Locate every blood parasite and identify its species.
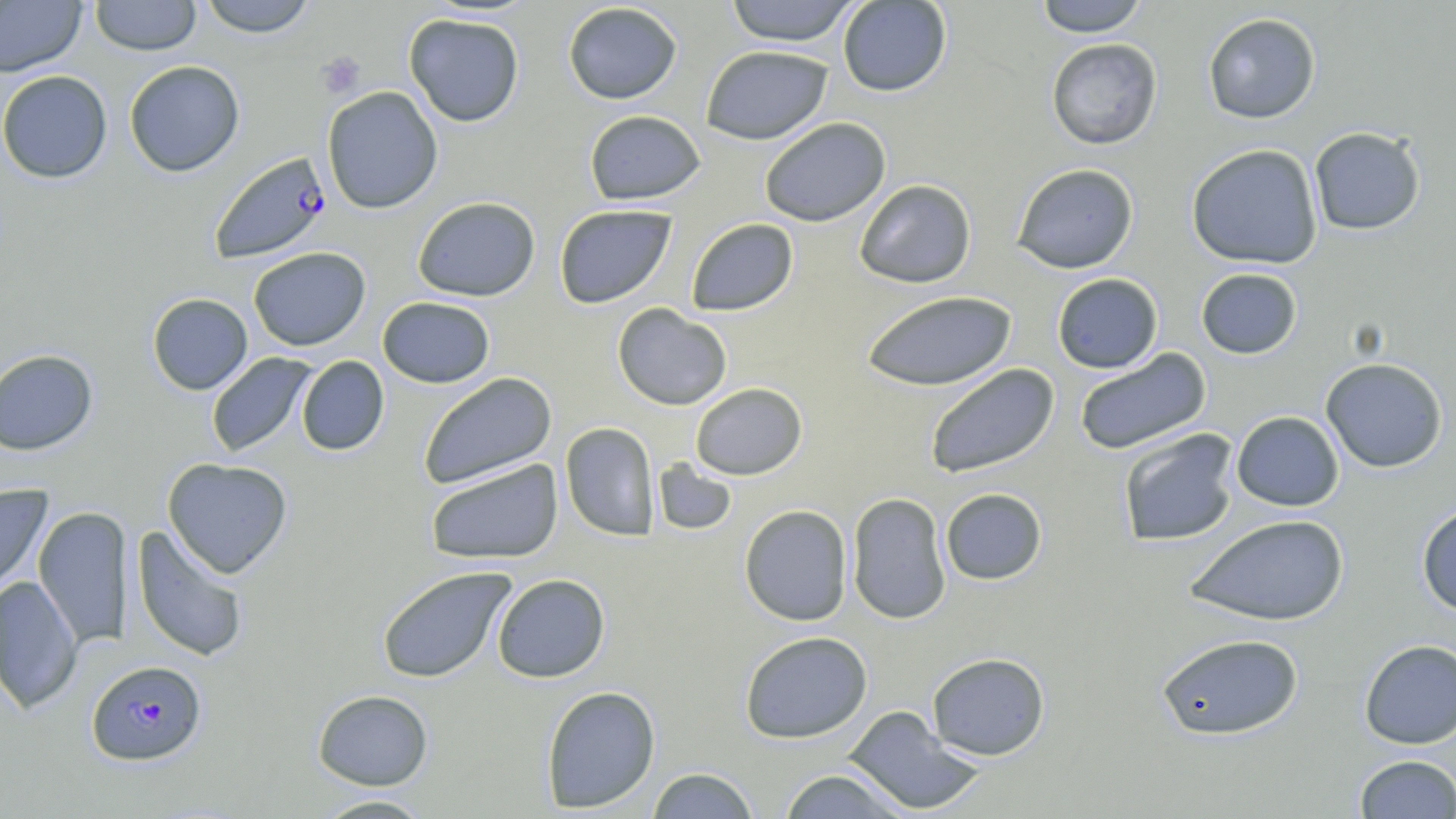
Approximate bounding boxes as named x1/y1/x2/y2 corners in pixels.
Plasmodium falciparum-infected red blood cells: (x1=208, y1=151, x2=332, y2=264), (x1=86, y1=660, x2=207, y2=766).
No Plasmodium ovale, Plasmodium malariae, Plasmodium vivax, Babesia divergens, or Trypanosoma brucei observed.

Platelet locations: (x1=317, y1=51, x2=366, y2=99). Uninfected red blood cell locations: (x1=89, y1=0, x2=202, y2=56), (x1=197, y1=0, x2=318, y2=37), (x1=724, y1=0, x2=860, y2=46), (x1=837, y1=0, x2=952, y2=97), (x1=1034, y1=0, x2=1150, y2=36), (x1=0, y1=1, x2=87, y2=77), (x1=562, y1=2, x2=683, y2=104), (x1=403, y1=12, x2=525, y2=127), (x1=1202, y1=12, x2=1321, y2=124), (x1=1046, y1=38, x2=1163, y2=150), (x1=700, y1=45, x2=833, y2=145), (x1=124, y1=60, x2=245, y2=177), (x1=0, y1=70, x2=113, y2=184), (x1=322, y1=86, x2=443, y2=214), (x1=583, y1=109, x2=706, y2=206), (x1=759, y1=117, x2=891, y2=227), (x1=1309, y1=126, x2=1427, y2=235), (x1=1186, y1=143, x2=1323, y2=270), (x1=1011, y1=163, x2=1139, y2=274), (x1=854, y1=179, x2=977, y2=288), (x1=412, y1=196, x2=541, y2=302), (x1=554, y1=204, x2=677, y2=309), (x1=686, y1=218, x2=799, y2=316), (x1=248, y1=247, x2=371, y2=351), (x1=1195, y1=267, x2=1303, y2=360), (x1=1051, y1=273, x2=1163, y2=374), (x1=861, y1=290, x2=1017, y2=392), (x1=147, y1=293, x2=253, y2=395), (x1=377, y1=296, x2=495, y2=388), (x1=612, y1=303, x2=732, y2=411), (x1=0, y1=348, x2=98, y2=455), (x1=1074, y1=348, x2=1212, y2=456), (x1=206, y1=352, x2=317, y2=457), (x1=296, y1=355, x2=389, y2=456), (x1=1320, y1=357, x2=1447, y2=473), (x1=924, y1=363, x2=1059, y2=480), (x1=418, y1=372, x2=558, y2=490), (x1=690, y1=382, x2=807, y2=480), (x1=1231, y1=410, x2=1344, y2=511), (x1=560, y1=422, x2=659, y2=541), (x1=1118, y1=428, x2=1240, y2=547), (x1=162, y1=458, x2=293, y2=578), (x1=425, y1=458, x2=563, y2=566), (x1=653, y1=459, x2=737, y2=537), (x1=0, y1=484, x2=53, y2=597), (x1=940, y1=487, x2=1048, y2=585), (x1=847, y1=492, x2=952, y2=625), (x1=1416, y1=503, x2=1456, y2=617), (x1=739, y1=504, x2=853, y2=626), (x1=34, y1=505, x2=133, y2=648), (x1=1185, y1=513, x2=1350, y2=626), (x1=131, y1=525, x2=250, y2=663), (x1=376, y1=565, x2=516, y2=684), (x1=492, y1=573, x2=610, y2=682), (x1=0, y1=576, x2=82, y2=714), (x1=739, y1=630, x2=873, y2=743), (x1=1155, y1=632, x2=1304, y2=741), (x1=1359, y1=639, x2=1456, y2=749), (x1=927, y1=652, x2=1050, y2=760), (x1=540, y1=685, x2=661, y2=813), (x1=312, y1=689, x2=433, y2=790), (x1=843, y1=705, x2=986, y2=816), (x1=1355, y1=754, x2=1456, y2=818), (x1=646, y1=767, x2=760, y2=818), (x1=776, y1=768, x2=912, y2=818), (x1=311, y1=794, x2=435, y2=818). Slide-level diagnosis: Plasmodium falciparum. One field of a larger specimen. Image is 1456×819 pixels. May-Grünwald-Giemsa-stained preparation. Thin blood film. Optical microscopy. Captured at 1000x magnification.